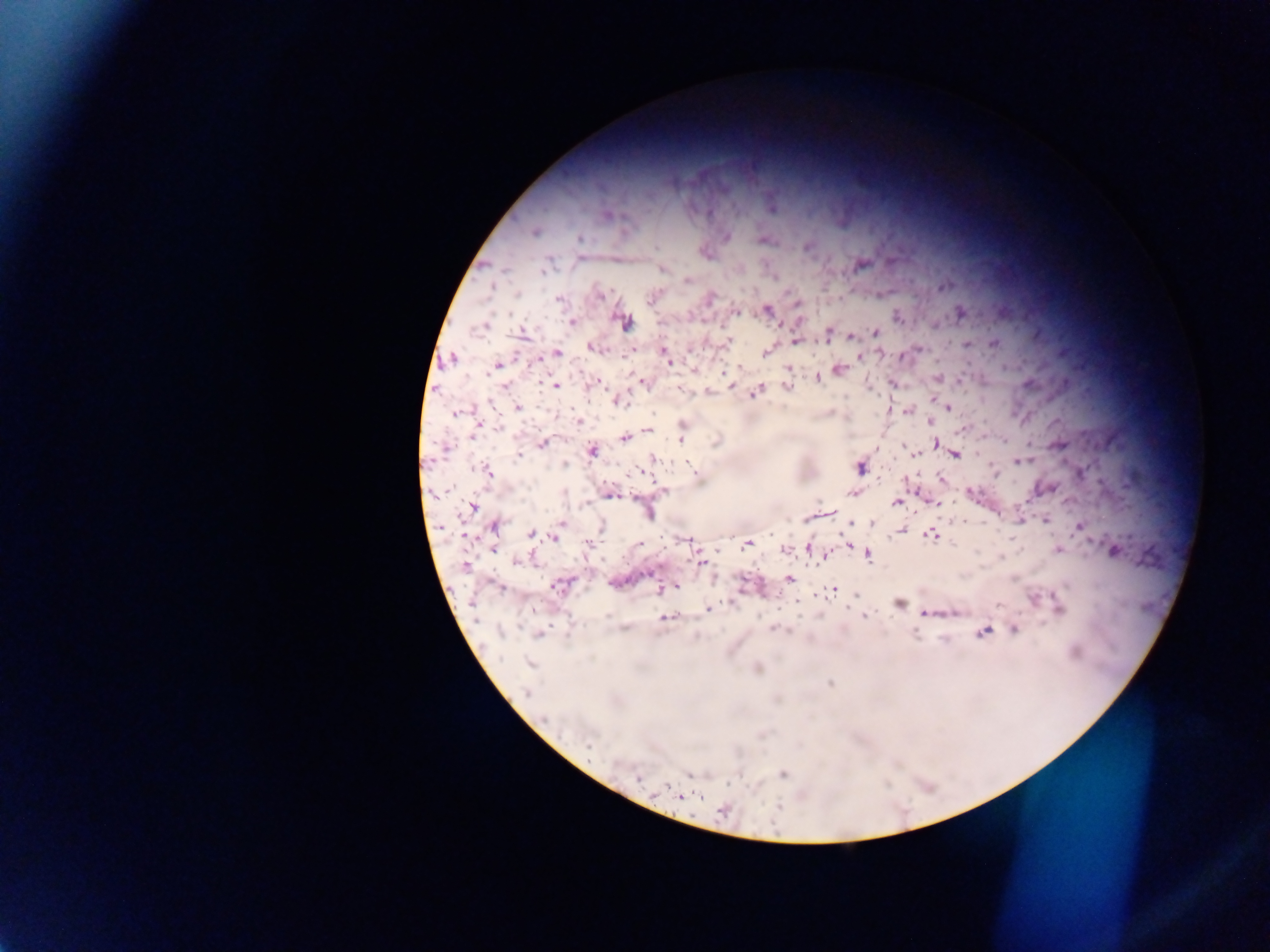
preparation = thick blood smear
field of view = single
capture = mobile-phone photograph through a microscope
Plasmodium parasite locations = approximate centers as [x, y] in pixels: [772, 207], [606, 214], [533, 232], [726, 237], [579, 239], [763, 239], [807, 246], [704, 252], [581, 257], [860, 264], [663, 268], [685, 279], [943, 285], [599, 294], [652, 297], [558, 298], [709, 298], [796, 304], [765, 309], [735, 311], [959, 312], [897, 317], [623, 321], [572, 322], [521, 332], [827, 332], [875, 332], [853, 336], [728, 340], [796, 340], [966, 343], [994, 343], [591, 347], [768, 350], [663, 351], [556, 353], [904, 354], [860, 355], [541, 358], [666, 358], [451, 359], [497, 365], [740, 367], [693, 368], [789, 368], [839, 369], [817, 376], [937, 377], [642, 381], [960, 381], [594, 383], [506, 385], [555, 385], [893, 385], [787, 386], [679, 388], [708, 391], [755, 391], [933, 399], [618, 400], [517, 407], [948, 407], [907, 409], [890, 410], [457, 412], [931, 421], [578, 422], [476, 425], [965, 426], [474, 431], [648, 431], [681, 434], [624, 438], [541, 443], [935, 444], [877, 448], [592, 450], [914, 454], [954, 454], [520, 455], [654, 459], [1019, 461], [565, 464], [859, 467], [487, 472], [940, 478], [1046, 488], [664, 490], [608, 492], [852, 492], [971, 493], [896, 502], [933, 502], [472, 507], [647, 512], [826, 513], [1046, 518], [1018, 519], [562, 523], [852, 523], [870, 523], [492, 525], [600, 527], [1079, 527], [902, 530], [531, 533], [555, 535], [931, 535], [465, 536], [686, 539], [747, 544], [848, 544], [493, 548], [810, 548], [785, 549], [1058, 549], [1114, 550], [825, 553], [867, 554], [519, 561], [700, 561], [464, 564], [789, 578], [558, 585], [675, 585], [834, 589], [659, 590], [854, 594], [898, 603], [1057, 608], [708, 609], [954, 612], [924, 613], [666, 616], [863, 616], [775, 628], [1013, 629], [982, 631], [538, 634], [528, 663], [757, 668], [829, 683], [526, 692], [782, 773], [690, 775], [637, 779], [680, 796], [723, 810]
country = Ghana
image size = 1270×952 pixels